Report the malaria status of this cell.
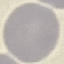
It is uninfected.

{
  "stain": "Giemsa",
  "capture": "smartphone through the microscope eyepiece",
  "image_type": "automatically extracted cell patch, resized to 64 × 64 pixels",
  "preparation": "thin blood film"
}